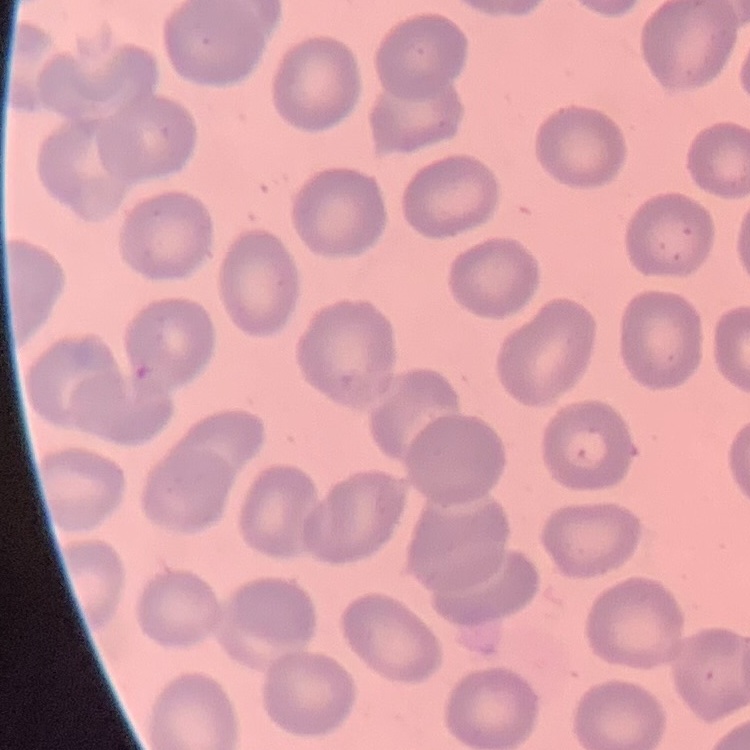
red_blood_cell_morphology: no rouleaux formation
stain: Field's or Giemsa
image_type: one tile cut from a larger photomicrograph
preparation: thin blood smear